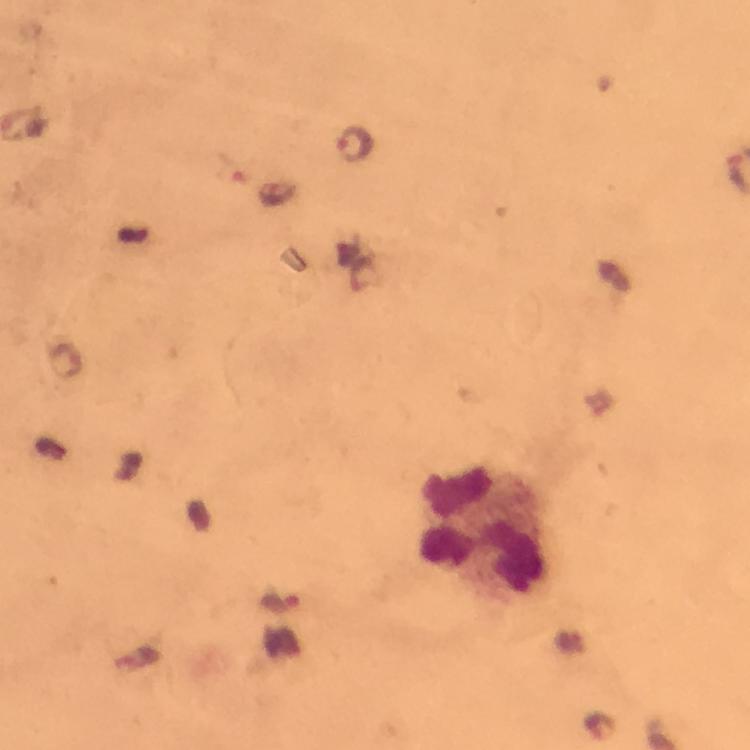
{
  "capture": "smartphone mounted on the microscope",
  "stain": "Giemsa",
  "malaria_parasite_locations": "approximate centers as [x, y] in pixels: [353, 143], [282, 602], [598, 726]",
  "leukocyte_locations": "approximate centers as [x, y] in pixels: [482, 534]",
  "image_size": "750×750 pixels",
  "magnification": "100x",
  "immersion_oil": "applied",
  "context": "from a malaria diagnostic workup",
  "preparation": "thick blood smear",
  "cropped_from": "a single field of view"
}